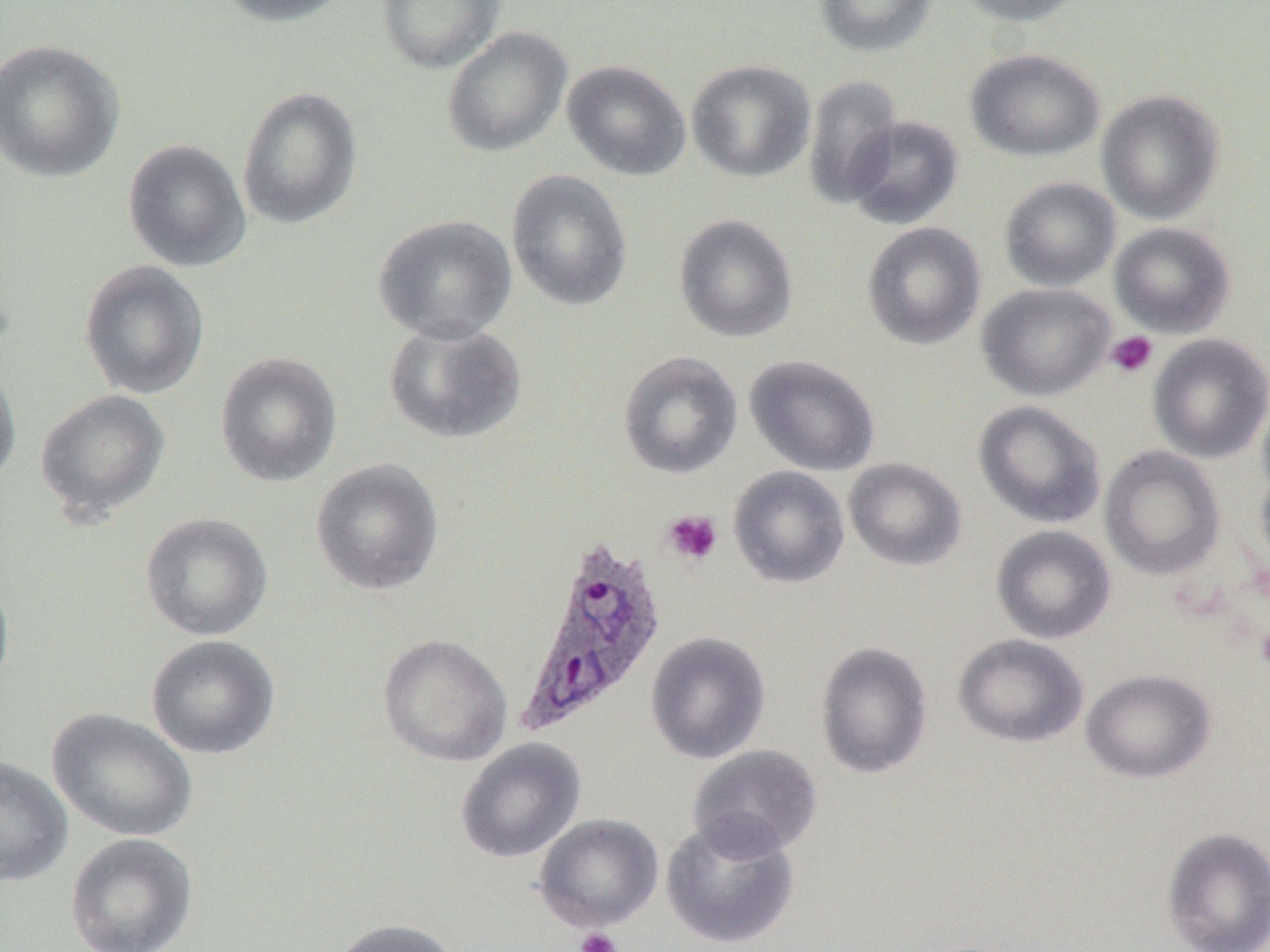
Approximate bounding boxes as (x1,y1)-(x2,y2) corner pairs in pixels. Uninfected red blood cell locations: (212,0)-(353,27), (375,0)-(506,74), (814,0)-(937,57), (952,0)-(1087,27), (441,26)-(572,158), (0,39)-(125,183), (965,48)-(1106,162), (686,59)-(816,183), (562,60)-(692,182), (802,74)-(902,209), (236,86)-(363,230), (1096,89)-(1225,224), (845,115)-(964,230), (122,139)-(251,272), (506,169)-(633,312), (999,177)-(1121,292), (674,214)-(798,343), (373,215)-(518,344), (862,222)-(986,350), (1109,222)-(1236,338), (79,260)-(210,399), (976,283)-(1115,401), (382,320)-(528,445), (1148,334)-(1270,464), (215,351)-(342,487), (618,351)-(743,479), (744,354)-(880,477), (0,359)-(22,491), (34,389)-(170,523), (1257,394)-(1270,507), (973,400)-(1106,529), (1099,445)-(1225,581), (843,457)-(967,571), (310,458)-(445,596), (1255,462)-(1270,579), (728,465)-(850,588), (140,512)-(273,641), (990,525)-(1116,644), (0,571)-(15,697), (645,631)-(771,764), (952,633)-(1089,748), (378,634)-(512,766), (146,635)-(280,760), (815,641)-(933,779), (1081,669)-(1216,784), (47,708)-(198,842), (455,738)-(586,863), (687,744)-(823,859), (0,755)-(73,887), (533,813)-(664,933), (661,815)-(800,950), (1161,827)-(1270,952), (65,833)-(199,952), (331,918)-(460,952). Plasmodium ovale-infected red blood cell locations: (514,536)-(667,738). Platelet locations: (1106,331)-(1158,378), (662,510)-(723,566), (575,926)-(622,952). Slide-level diagnosis: Plasmodium ovale. Optical microscopy. 1000x magnification. Thin blood film. Image is 1270×952 pixels. Single field of view.